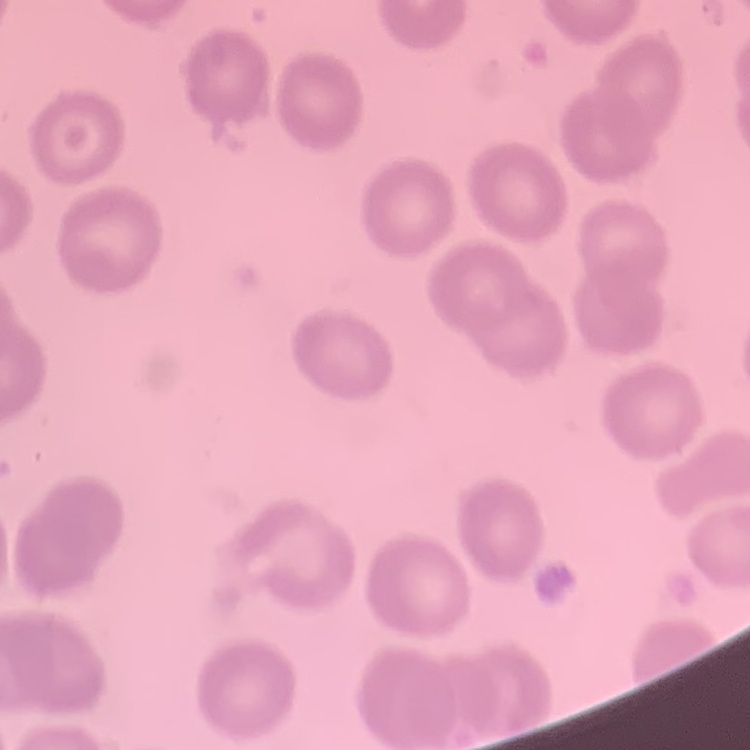

The erythrocytes show no rouleaux formation. Thin peripheral smear. Stained with either Field's or Giemsa. Square crop of a larger photomicrograph.